Assess this cell for malaria.
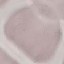

It is uninfected.

preparation: thin smear
image_type: automatically extracted cell patch, resized to 64 × 64 pixels
stain: Giemsa
capture: smartphone through the microscope eyepiece